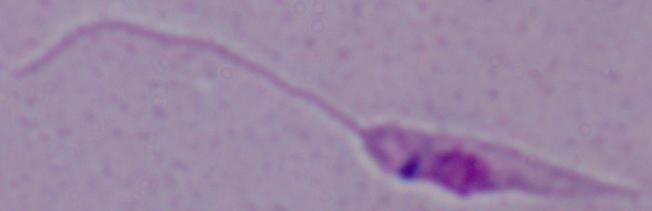
magnification: 1000x
modality: micrograph
identification: Leishmania